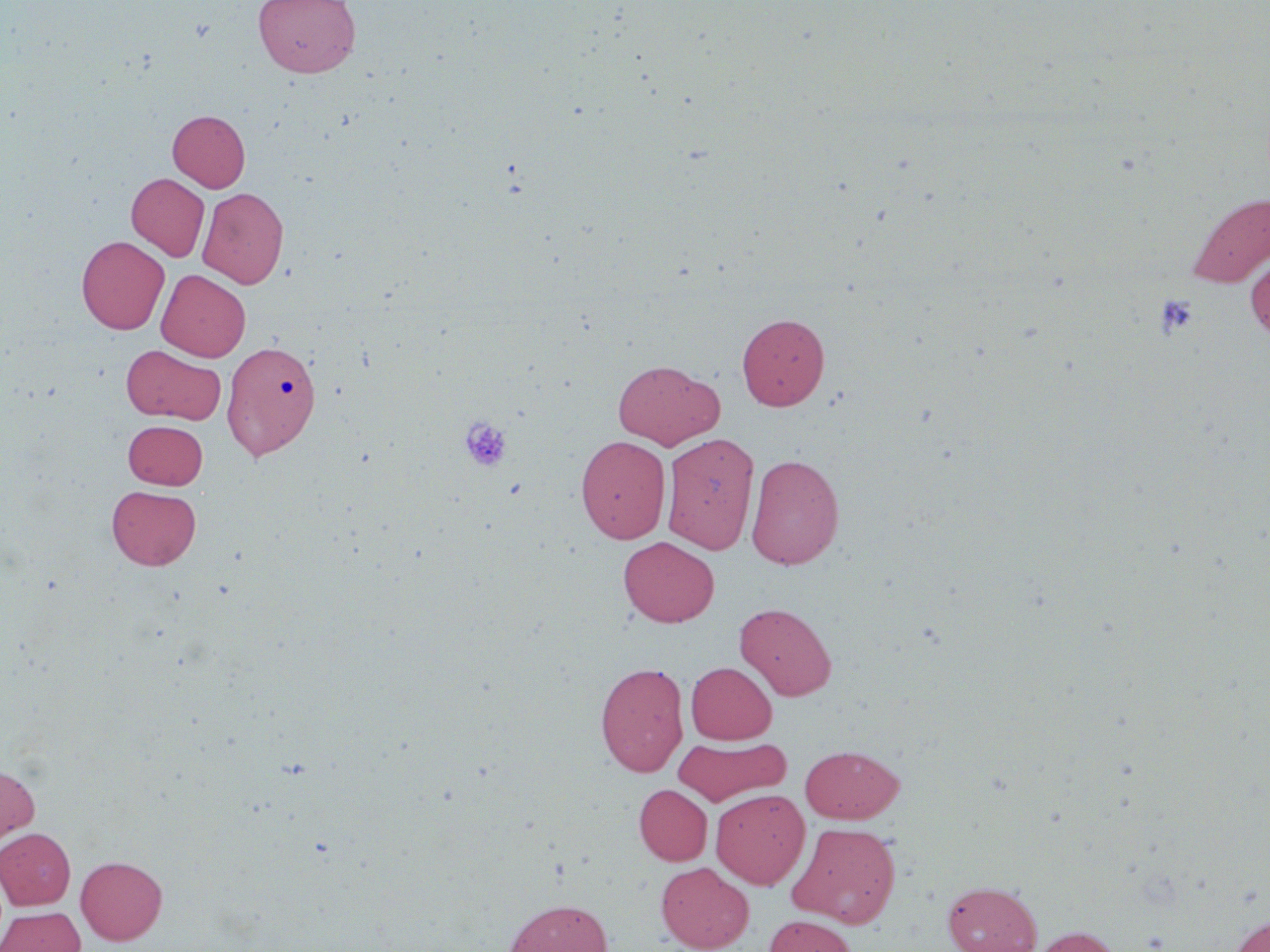

Approximate bounding boxes as [x1, y1, x2, y2] in pixels. Uninfected red blood cell locations: [252, 0, 361, 77], [168, 110, 250, 192], [126, 173, 209, 261], [198, 187, 288, 288], [1186, 192, 1270, 287], [77, 235, 170, 334], [1245, 252, 1270, 340], [156, 269, 250, 361], [737, 312, 830, 410], [222, 339, 322, 461], [121, 345, 226, 424], [612, 359, 724, 449], [123, 420, 208, 489], [661, 432, 759, 554], [575, 435, 671, 544], [745, 453, 845, 569], [107, 484, 201, 570], [618, 536, 720, 627], [735, 602, 837, 700], [595, 661, 689, 777], [686, 662, 777, 744], [673, 735, 790, 806], [800, 744, 904, 823], [0, 764, 39, 849], [634, 784, 712, 865], [710, 788, 810, 889], [787, 822, 902, 927], [0, 828, 75, 910], [76, 856, 168, 945], [656, 862, 754, 952], [942, 880, 1042, 952], [504, 898, 612, 952], [0, 907, 85, 952], [1225, 913, 1270, 952], [764, 915, 857, 952], [1029, 925, 1124, 952]. Platelet locations: [1155, 294, 1198, 337], [459, 416, 512, 473]. Slide-level diagnosis: negative for blood parasites. One field of a larger specimen. Image is 1270×952 pixels. May-Grünwald-Giemsa-stained preparation. Thin blood smear. Captured at 1000x magnification. Light microscopy.